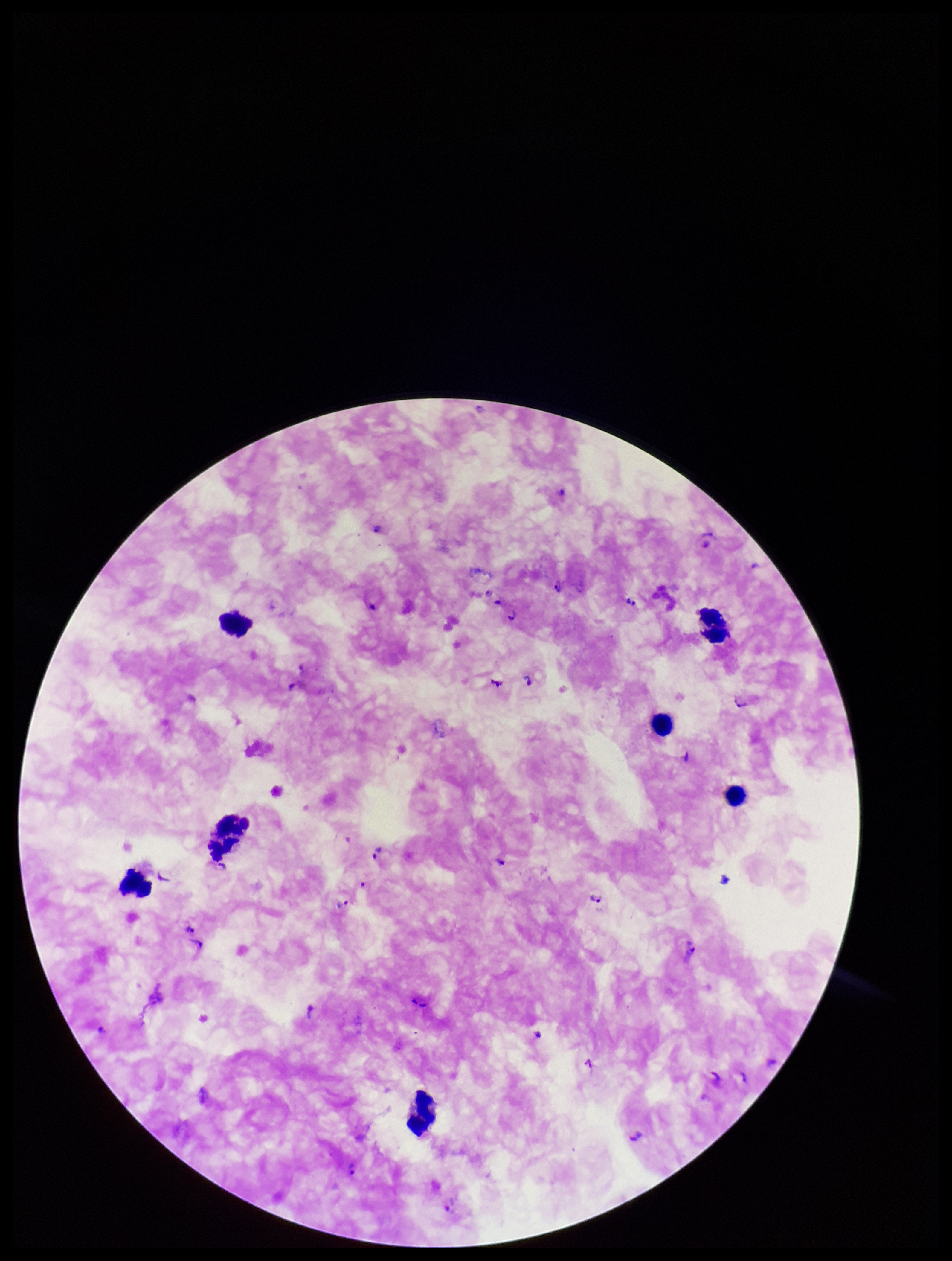

Summary:
  - Preparation: thick smear
  - Plasmodium parasites: detected
  - Image size: 952×1261 pixels
  - Leukocyte count: 7
  - Parasite count: 30
  - Field of view: single
  - Stain: Giemsa
  - Capture: smartphone photograph through the microscope eyepiece
  - Patient malaria status: infected
  - Species reported for this patient: Plasmodium falciparum